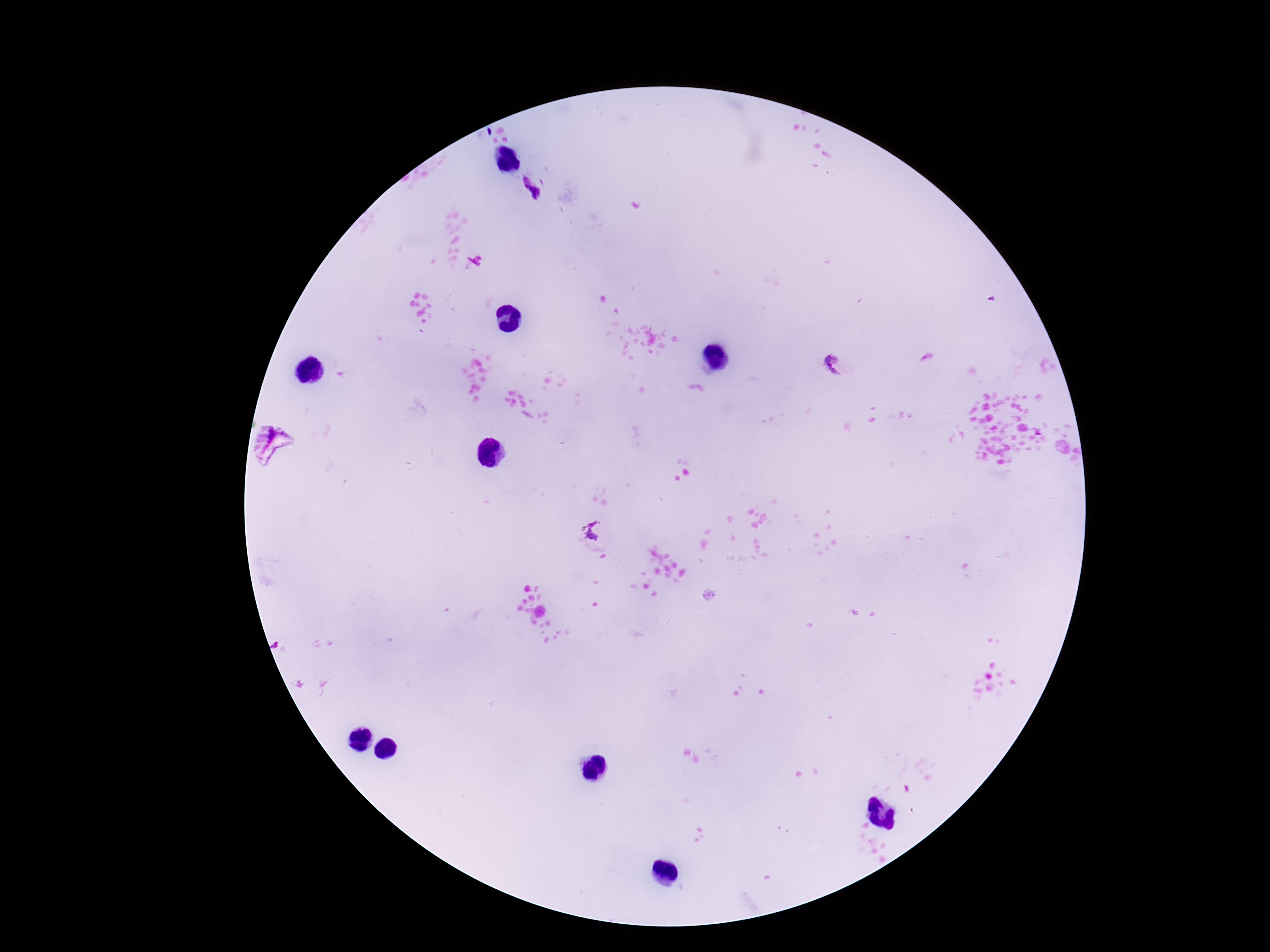

magnification = 100x
capture = smartphone camera through the microscope eyepiece
preparation = thick blood film
stain = Giemsa
field of view = one from this slide
patient malaria status = infected
Plasmodium parasite locations = approximate object centers, in pixels from the top-left corner: (x=530, y=189), (x=836, y=365), (x=591, y=529)
image size = 1270×952 pixels